Assess for malaria.
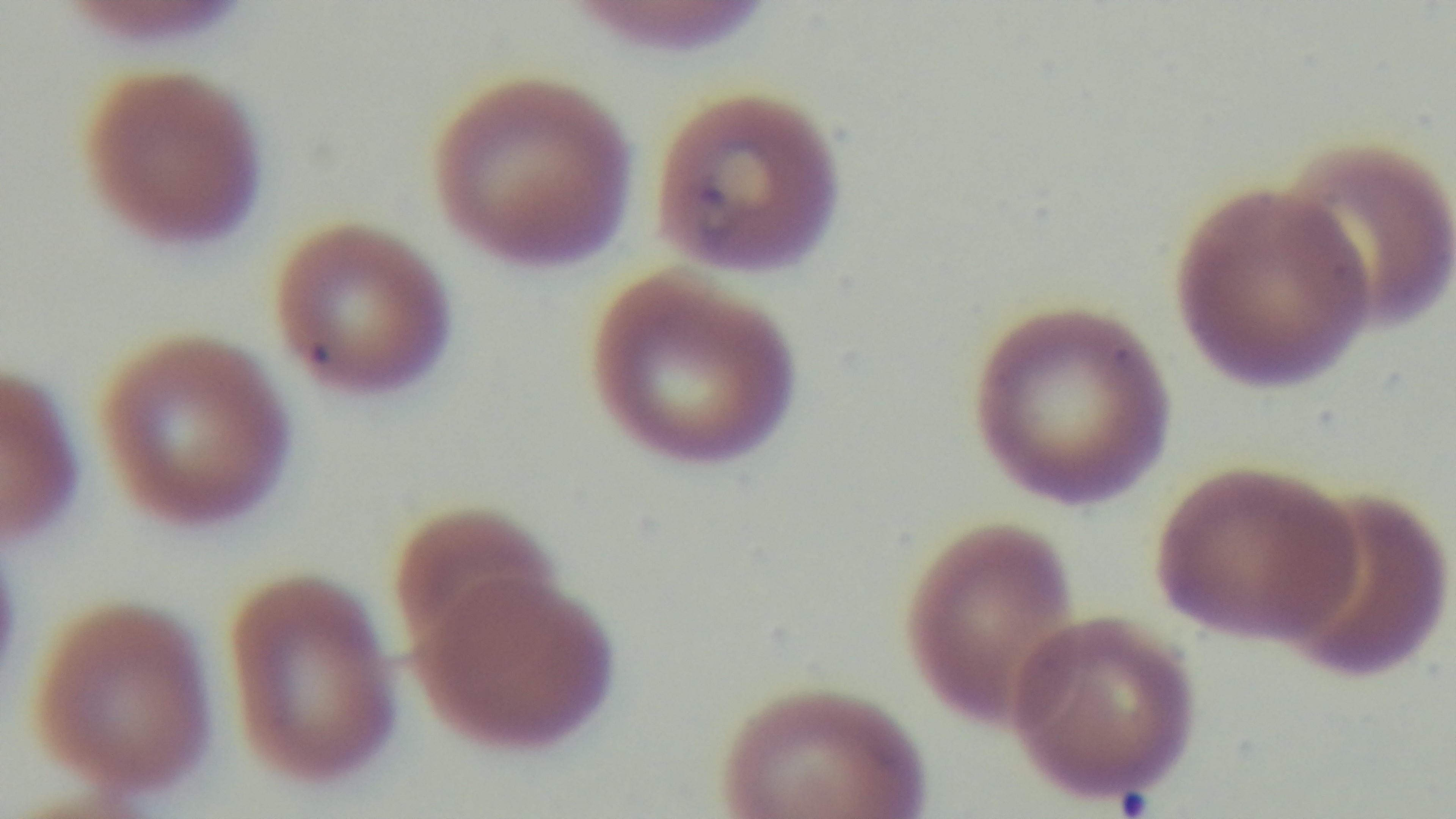

Positive.

field of view = one from the slide
objective = 100x oil immersion
modality = light microscopy
preparation = thin smear
stain = Giemsa
capture = mounted 4K digital camera